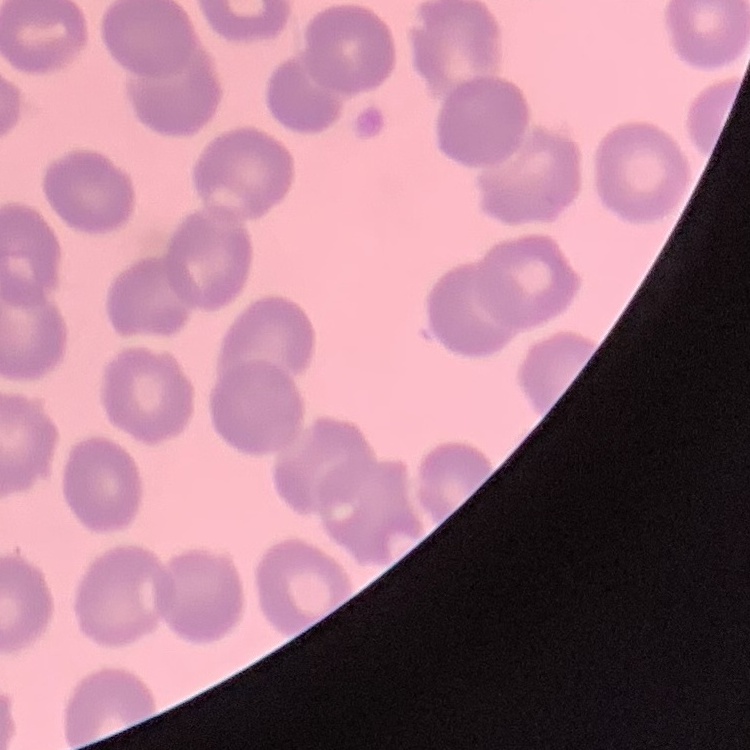 The erythrocytes exhibit no rouleaux formation. Thin peripheral smear. Stained with either Field's or Giemsa. Square crop of a larger photomicrograph.